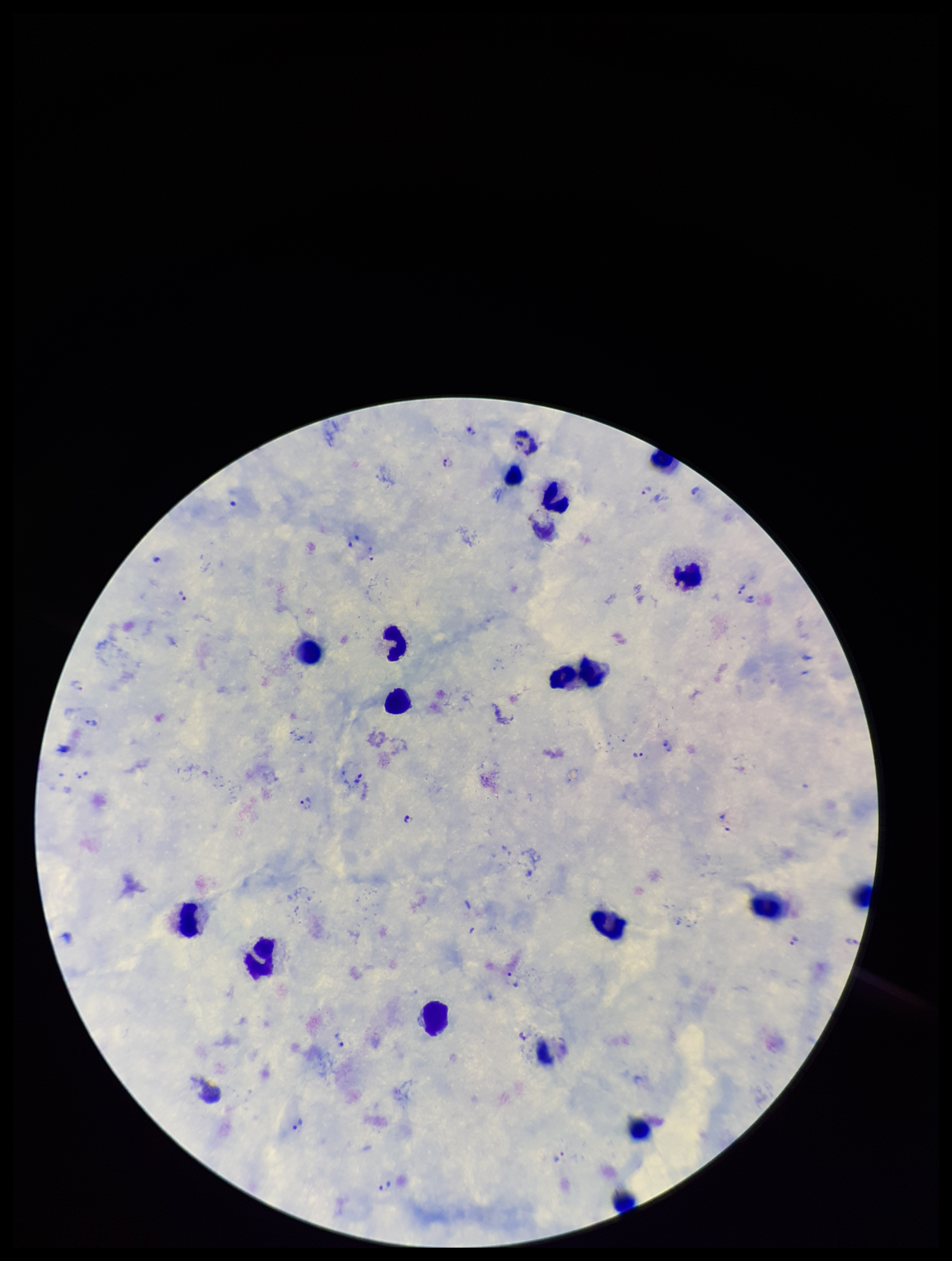

Summary:
  - Image size: 952×1261 pixels
  - Plasmodium parasites: identified
  - Leukocyte count: 16
  - Field of view: single
  - Patient malaria status: infected
  - Preparation: thick blood smear
  - Capture: smartphone photograph through the microscope eyepiece
  - Stain: Giemsa
  - Species reported for this patient: Plasmodium vivax
  - Parasite count: 15